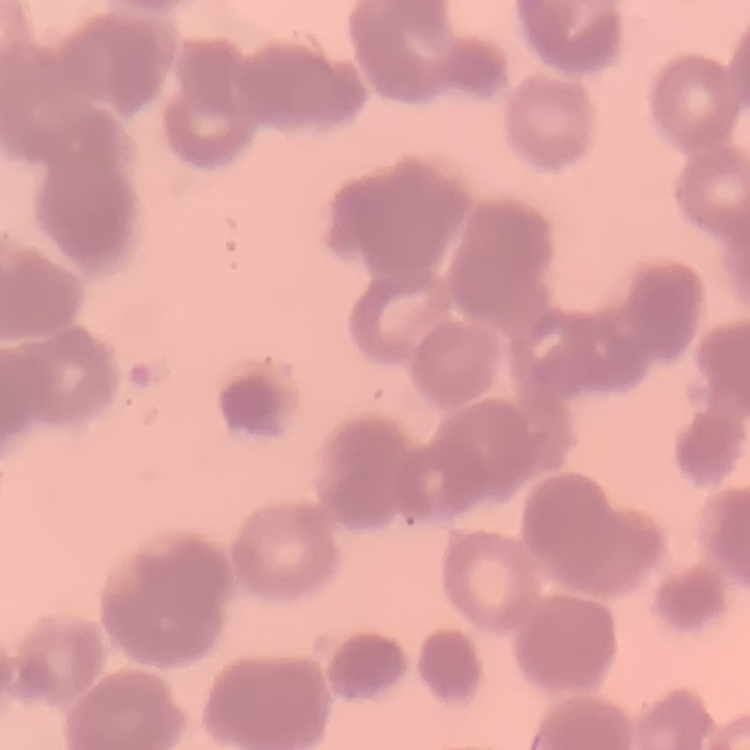
{
  "red_blood_cell_morphology": "rouleaux formation",
  "preparation": "thin peripheral smear",
  "image_type": "square crop of a larger photomicrograph",
  "stain": "Field's or Giemsa"
}